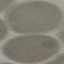
malaria status = uninfected
capture = smartphone camera at the microscope eyepiece
image type = automatically extracted cell patch, resized to 64 × 64 pixels
preparation = thin blood film
stain = Giemsa